Name the blood parasite species.
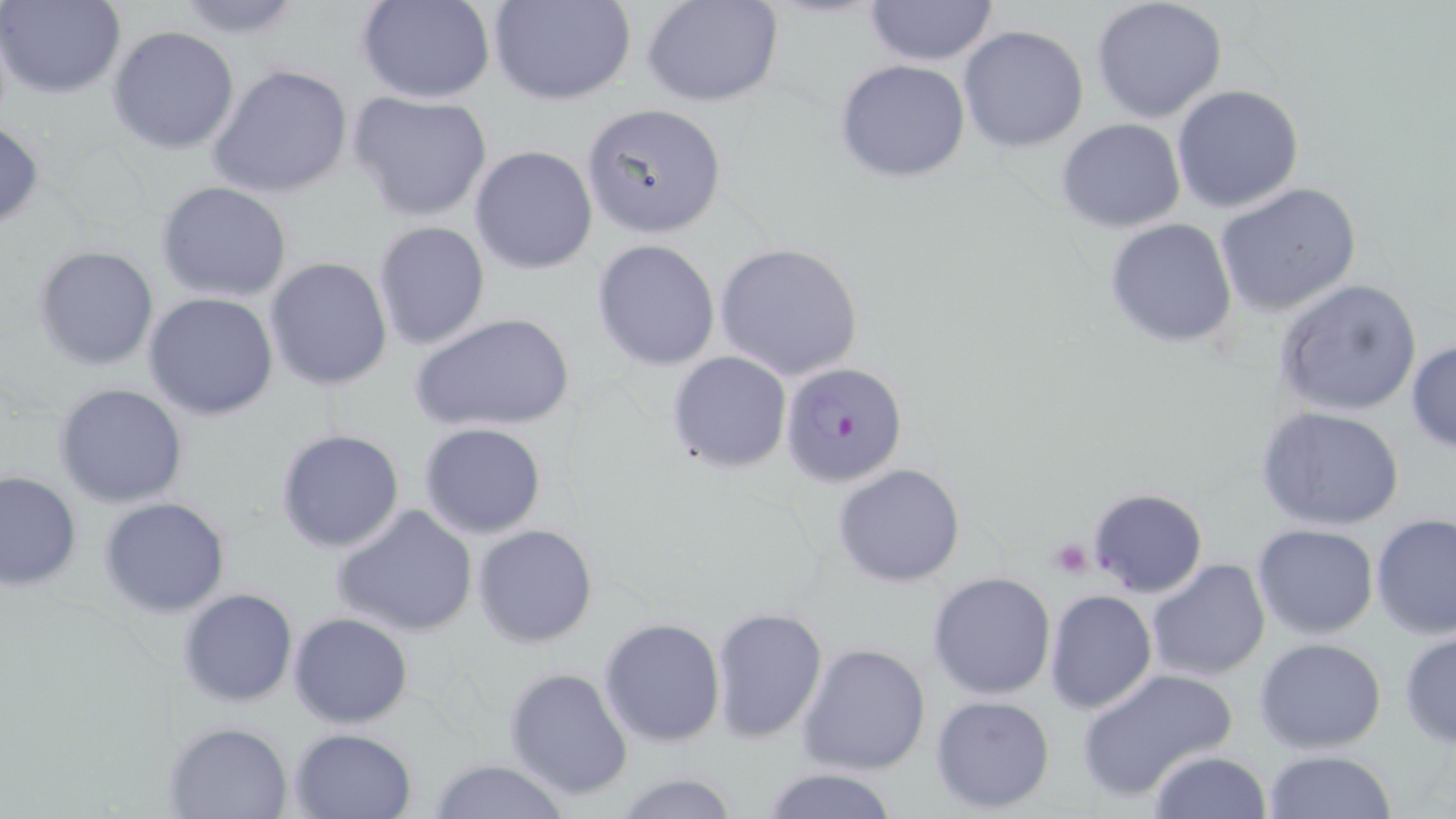
Plasmodium falciparum.

platelet locations = approximate bounding boxes as (x1,y1)-(x2,y2) corner pairs in pixels: (1050,537)-(1096,578)
Plasmodium falciparum-infected red blood cell locations = approximate bounding boxes as (x1,y1)-(x2,y2) corner pairs in pixels: (781,360)-(909,488), (1086,487)-(1208,598)
uninfected red blood cell locations = approximate bounding boxes as (x1,y1)-(x2,y2) corner pairs in pixels: (0,0)-(127,100), (170,0)-(308,38), (356,0)-(497,104), (491,0)-(637,106), (642,0)-(784,106), (864,0)-(1000,67), (1090,0)-(1229,122), (958,25)-(1090,153), (108,26)-(239,155), (834,58)-(971,183), (208,63)-(353,199), (1172,84)-(1305,213), (348,91)-(494,222), (580,102)-(728,238), (0,116)-(44,232), (1056,118)-(1187,234), (470,146)-(599,274), (156,181)-(294,302), (1214,182)-(1362,317), (1104,218)-(1239,348), (373,221)-(490,350), (592,239)-(722,371), (714,241)-(864,381), (34,245)-(159,370), (265,257)-(394,392), (1273,277)-(1424,418), (144,293)-(280,421), (409,311)-(576,434), (1406,339)-(1456,452), (666,350)-(793,472), (54,383)-(190,507), (1257,407)-(1405,532), (418,422)-(548,538), (275,428)-(405,553), (833,463)-(964,587), (0,470)-(81,593), (98,496)-(230,617), (332,503)-(480,637), (1371,513)-(1456,641), (472,524)-(598,648), (1252,524)-(1380,640), (1146,558)-(1272,681), (927,571)-(1056,701), (177,588)-(299,708), (1044,591)-(1156,712), (708,605)-(828,743), (288,613)-(414,728), (598,617)-(726,746), (1399,629)-(1456,748), (1253,636)-(1388,753), (797,642)-(931,776), (504,667)-(634,803), (1076,667)-(1237,803), (930,695)-(1056,811), (164,721)-(295,817), (289,728)-(416,819), (1148,749)-(1270,818), (1264,749)-(1398,819), (425,759)-(571,818), (755,767)-(902,819), (612,773)-(742,818)
magnification = 1000x
modality = light microscopy
image size = 1456×819 pixels
field of view = one of a larger specimen
stain = May-Grünwald-Giemsa
preparation = thin blood smear